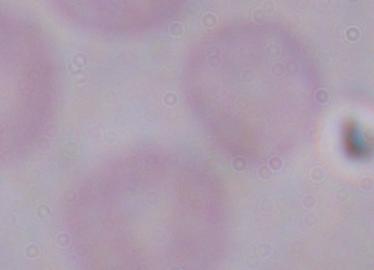

identification = trypanosome
magnification = 1000x
modality = micrograph